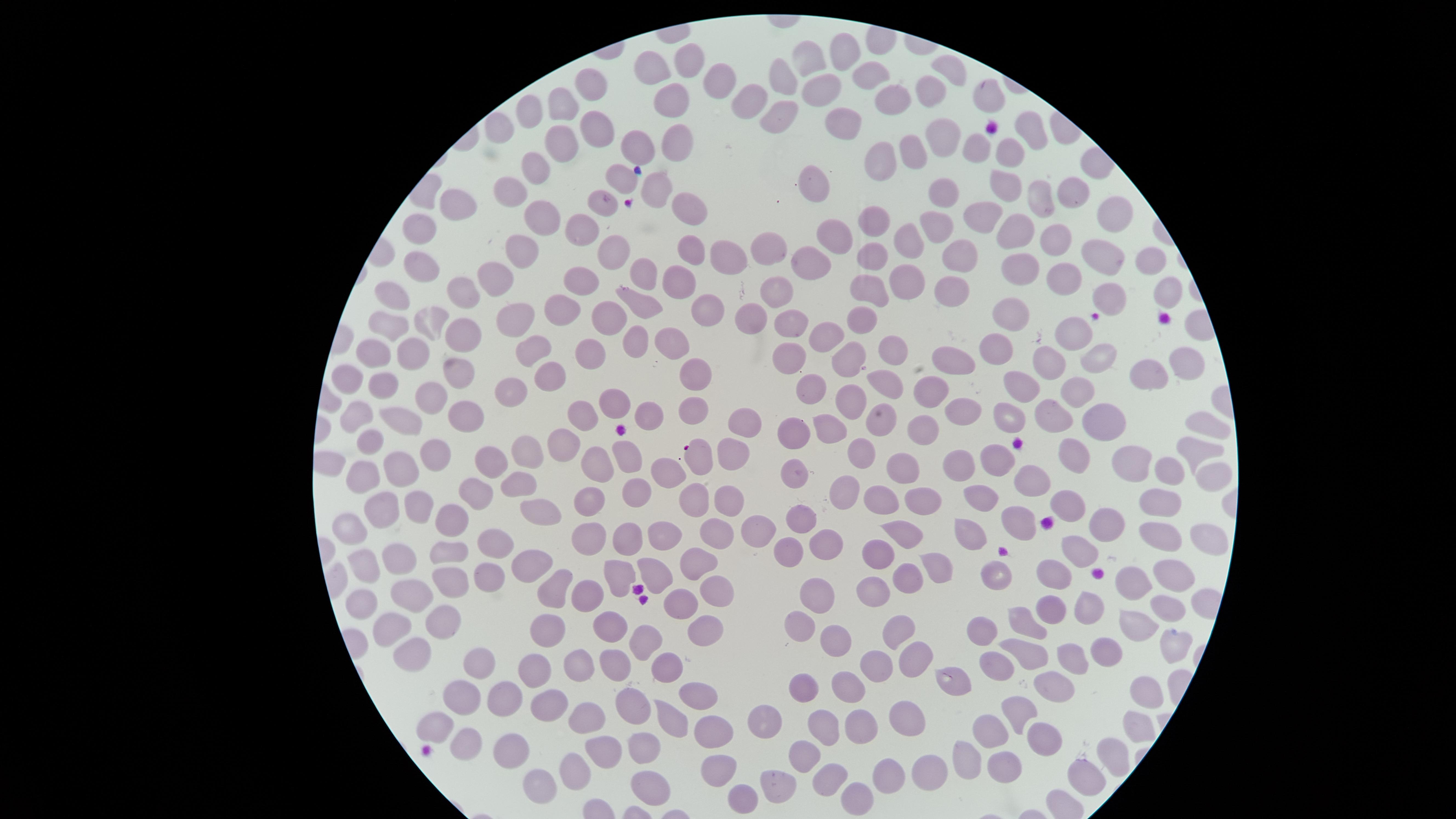
uninfected_red_blood_cells: 'approximate marker points as [x, y] in pixels: [844, 50], [689, 58], [809, 58], [657, 73], [952, 73], [869, 74], [721, 79], [788, 79], [591, 85], [931, 87], [822, 90], [753, 98], [985, 98], [890, 99], [671, 103], [560, 106], [779, 110], [530, 113], [848, 122], [1032, 127], [600, 130], [498, 132], [556, 140], [639, 142], [928, 142], [673, 143], [978, 143], [1008, 144], [912, 152], [878, 160], [535, 165], [619, 174], [1009, 180], [810, 188], [656, 191], [1070, 192], [939, 193], [510, 195], [1036, 199], [602, 202], [457, 203], [691, 207], [987, 213], [1110, 213], [544, 216], [876, 222], [934, 223], [581, 229], [421, 231], [1017, 233], [1052, 235], [906, 237], [837, 241], [689, 246], [614, 247], [770, 248], [522, 250], [875, 255], [1103, 255], [721, 260], [960, 260], [1148, 260], [418, 265], [808, 266], [1023, 267], [645, 270], [1063, 273], [904, 279], [498, 280], [585, 281], [681, 281], [865, 282], [778, 290], [1169, 290], [463, 292], [391, 295], [951, 296], [1104, 296], [638, 300], [563, 311], [706, 311], [1008, 313], [864, 316], [517, 317], [435, 319], [608, 319], [753, 321], [390, 323], [793, 326], [1073, 331], [457, 332], [833, 332], [633, 340], [673, 344], [411, 347], [372, 350], [532, 350], [893, 350], [588, 352], [1003, 352], [1094, 356], [956, 359], [794, 360], [844, 360], [1177, 361], [457, 364], [1049, 364], [1144, 370], [552, 371], [698, 375], [350, 378], [1022, 381], [888, 385], [385, 389], [814, 389], [1073, 389], [514, 391], [850, 393], [435, 394], [929, 394], [619, 397], [691, 409], [1053, 411], [356, 412], [645, 412], [963, 414], [591, 417], [1009, 417], [467, 419], [404, 420], [882, 421], [744, 423], [1102, 423], [1201, 423], [927, 424], [796, 431], [828, 431], [373, 440], [566, 441], [1193, 446], [437, 450], [531, 450], [1075, 452], [627, 454], [861, 455], [726, 456], [998, 459], [602, 460], [966, 460], [695, 461], [492, 463], [1129, 464], [904, 467], [400, 468], [664, 469], [1164, 469], [793, 472], [1211, 472], [364, 473], [1036, 480], [523, 481], [853, 489], [635, 492], [885, 495], [478, 497], [593, 497], [981, 497], [923, 499], [1157, 499], [696, 500], [1073, 500], [419, 503], [735, 504], [543, 513], [1014, 514], [382, 516], [453, 516], [802, 518], [1105, 519], [587, 525], [757, 528], [969, 530], [352, 531], [629, 531], [712, 531], [903, 531], [1158, 533], [664, 534], [1206, 539], [494, 544], [785, 546], [823, 548], [1077, 551], [448, 552], [876, 556], [398, 557], [523, 564], [696, 564], [939, 564], [369, 565], [656, 566], [1173, 569], [613, 573], [1059, 573], [907, 575], [993, 577], [1136, 579], [483, 580], [556, 583], [708, 584], [444, 585], [877, 591], [417, 596], [587, 597], [814, 597], [683, 598], [364, 600], [1161, 602], [1055, 608], [1085, 610], [444, 619], [802, 619], [705, 620], [983, 622], [1030, 622], [1132, 623], [393, 624], [554, 625], [608, 626], [898, 629], [834, 636], [648, 638], [1164, 644], [1027, 648], [414, 652], [914, 653], [581, 656], [1067, 656], [1098, 657], [478, 661], [999, 665], [612, 666], [670, 667], [537, 668], [878, 669], [849, 679], [947, 679], [1058, 680], [810, 686], [1143, 692], [506, 694], [697, 694], [468, 702], [637, 703], [549, 706], [1023, 706], [902, 712], [593, 719], [671, 719], [769, 720], [863, 723], [436, 725], [824, 725], [1135, 727], [718, 731], [990, 731], [1046, 732], [462, 740], [510, 745], [602, 748], [644, 750], [1115, 750], [808, 752], [963, 759], [1002, 762], [575, 769], [718, 769], [927, 769], [889, 773], [1088, 773], [827, 778], [776, 779], [544, 784], [652, 787], [858, 794], [746, 795]'
image_size: 1456×819 pixels
presence: no malaria parasites detected
stain: Giemsa
field_of_view: single
visible_region: circular
capture: smartphone photograph through the microscope eyepiece
preparation: thin blood film